Assess this cell for malaria.
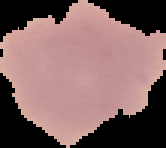

Uninfected.

image_size: 166×148 pixels
preparation: thin blood film
image_type: segmented cell region on a black background